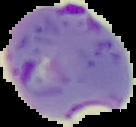

image size = 136×127 pixels
malaria status = parasitized
image type = segmented cell region with the area outside set to black
preparation = thin blood smear